Assess this cell for malaria.
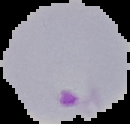
It is parasitized.

Summary:
  - Preparation: thin blood smear
  - Image size: 130×124 pixels
  - Image type: segmented cell region with the area outside set to black